Identify the preparation type.
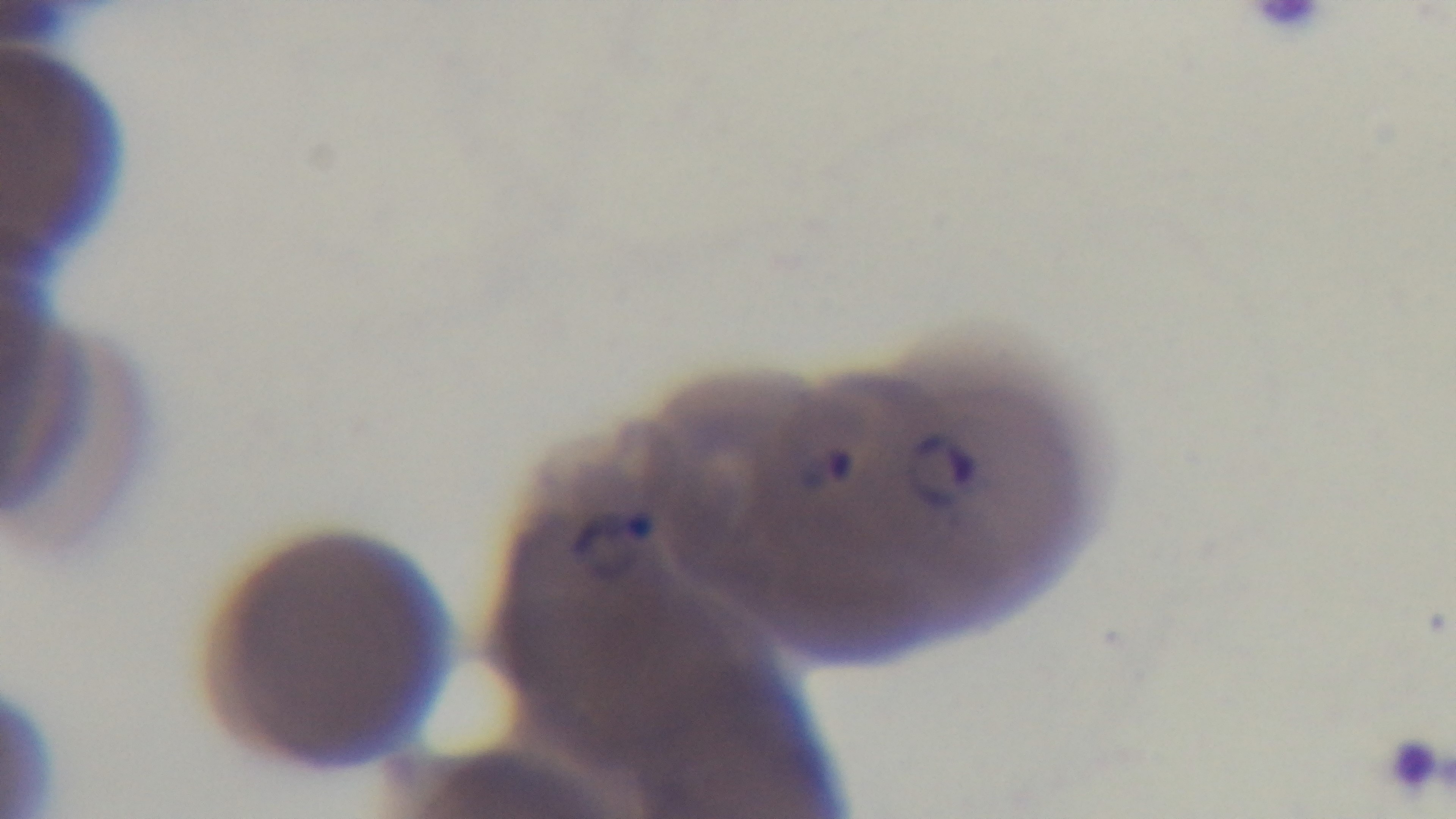

Thin.

Giemsa stain. One field from the slide. Malaria status: positive. Captured with a mounted 4K digital camera. 100x oil-immersion objective. Photomicrograph.